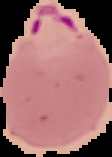
Cell region segmented out of the field of view; the surrounding area is masked to black. Image is 112×157 pixels. From a thin blood film. Malaria status: parasitized.